Identify the blood parasite species.
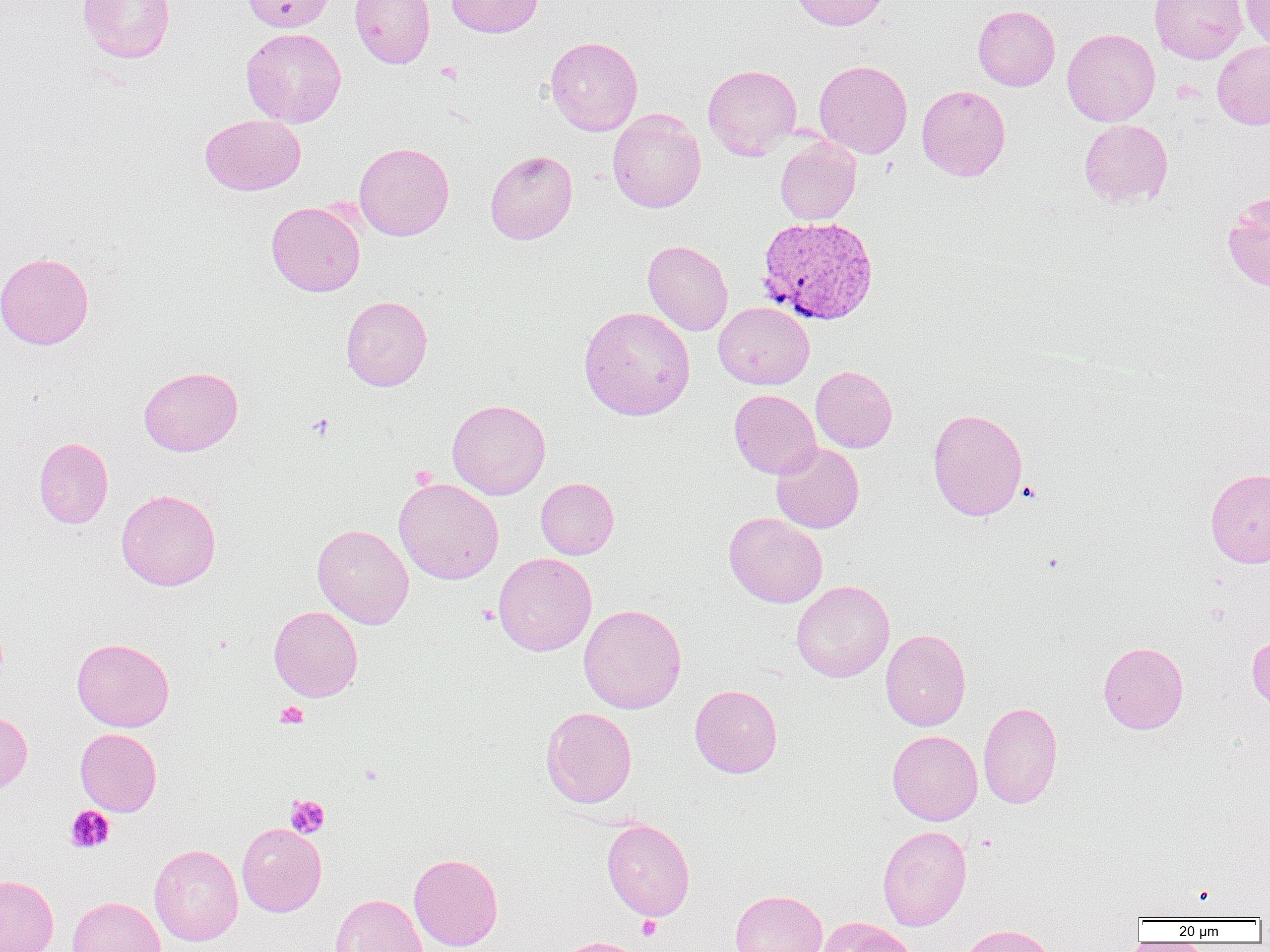
Plasmodium vivax.

Approximate bounding boxes as (x1, y1, x2, y2) in pixels. Uninfected red blood cell locations: (77, 0, 175, 63), (241, 0, 336, 32), (349, 0, 435, 68), (446, 0, 544, 38), (790, 0, 892, 31), (1149, 0, 1247, 64), (1240, 0, 1270, 52), (973, 5, 1060, 91), (241, 28, 346, 128), (1062, 28, 1160, 126), (545, 36, 643, 135), (1212, 40, 1270, 130), (814, 60, 913, 158), (703, 64, 801, 159), (917, 85, 1010, 181), (607, 109, 706, 213), (200, 115, 305, 196), (1079, 119, 1173, 207), (774, 137, 861, 225), (354, 142, 454, 240), (485, 150, 577, 244), (1222, 191, 1270, 292), (266, 201, 365, 297), (643, 240, 733, 335), (0, 252, 94, 350), (341, 295, 432, 391), (714, 302, 814, 390), (579, 306, 695, 421), (811, 365, 897, 453), (139, 366, 243, 456), (729, 389, 821, 479), (447, 399, 550, 500), (927, 407, 1028, 521), (34, 437, 113, 528), (770, 442, 864, 533), (1205, 468, 1270, 568), (536, 477, 619, 559), (394, 478, 504, 584), (116, 489, 221, 590), (724, 512, 827, 608), (312, 524, 414, 629), (493, 552, 596, 656), (791, 580, 894, 682), (578, 603, 687, 714), (268, 606, 363, 701), (880, 628, 971, 731), (1247, 632, 1270, 711), (72, 638, 174, 731), (1098, 641, 1188, 734), (690, 684, 782, 778), (978, 701, 1063, 809), (541, 707, 637, 808), (0, 710, 32, 796), (75, 728, 162, 816), (887, 730, 983, 825), (601, 818, 695, 921), (237, 822, 327, 916), (877, 825, 972, 931), (149, 844, 243, 945), (409, 853, 503, 951), (0, 875, 58, 952), (730, 890, 827, 952), (331, 894, 427, 952), (67, 896, 166, 952), (817, 917, 918, 952), (955, 924, 1059, 952), (553, 936, 649, 952). Platelet locations: (435, 62, 463, 85), (307, 413, 335, 441), (1017, 481, 1043, 504), (476, 605, 499, 624), (275, 701, 308, 728), (285, 794, 330, 838), (65, 806, 114, 853), (637, 915, 662, 940). Plasmodium vivax-infected red blood cell locations: (756, 215, 879, 325). One field of a larger specimen. Thin blood film. Image is 1270×952 pixels. Light microscopy. Captured at 1000x magnification.